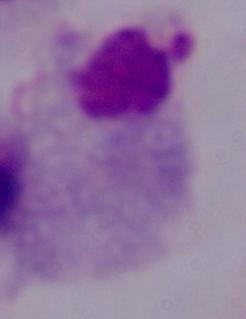

magnification: 1000x
identification: trichomonad
modality: photomicrograph